Describe the morphology of the erythrocytes.
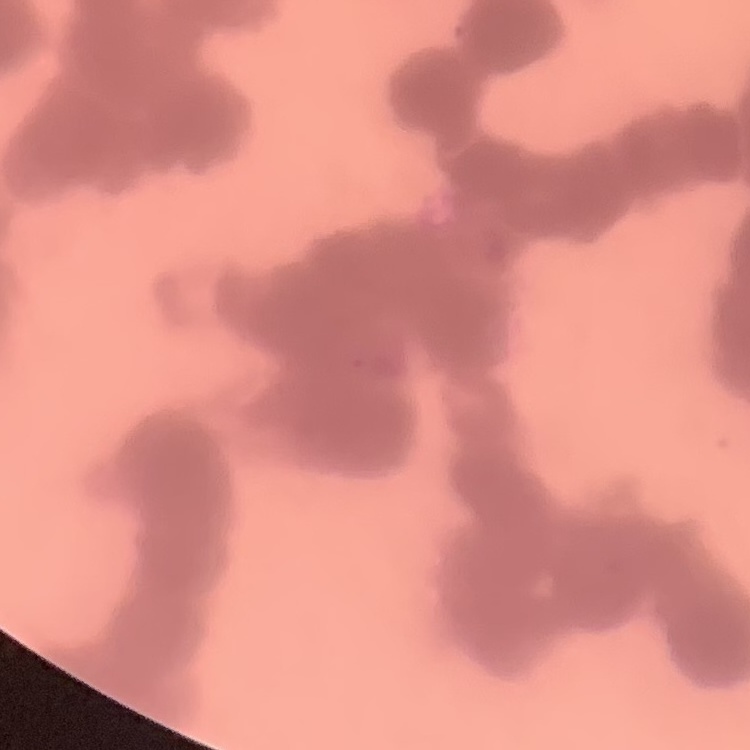

They show rouleaux formation.

Stained with either Field's or Giemsa. One tile cut from a larger photomicrograph. Thin peripheral smear.